Locate every blood parasite and identify its species.
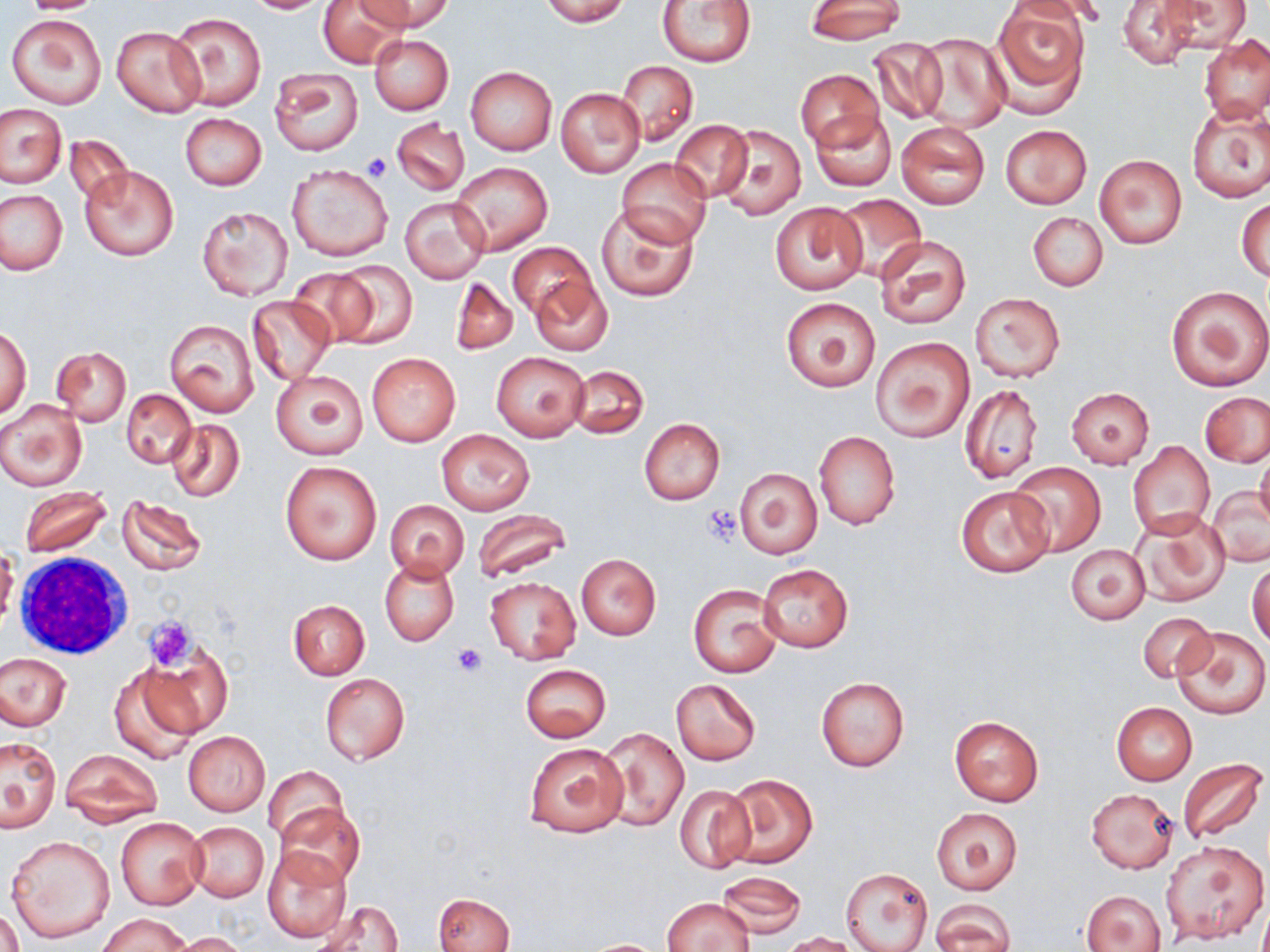

No blood parasites observed.

Approximate bounding boxes as [x1, y1, x2, y2] in pixels. Uninfected red blood cell locations: [18, 0, 105, 13], [242, 0, 334, 14], [363, 0, 452, 34], [538, 0, 629, 26], [806, 0, 905, 44], [992, 0, 1091, 107], [1004, 0, 1111, 27], [1117, 0, 1204, 70], [1160, 0, 1250, 53], [318, 1, 404, 68], [656, 1, 758, 68], [169, 12, 268, 111], [6, 13, 107, 108], [112, 26, 206, 117], [1200, 33, 1270, 123], [369, 34, 452, 116], [917, 34, 1008, 132], [868, 36, 949, 125], [617, 60, 697, 145], [466, 66, 556, 155], [270, 68, 364, 156], [796, 70, 883, 149], [557, 88, 645, 177], [1187, 103, 1270, 202], [1, 105, 65, 188], [811, 110, 897, 193], [180, 113, 266, 190], [392, 118, 471, 196], [669, 119, 754, 204], [895, 121, 989, 209], [713, 124, 807, 220], [999, 124, 1092, 210], [65, 134, 134, 209], [1093, 153, 1187, 248], [616, 157, 713, 249], [451, 162, 553, 255], [286, 163, 395, 262], [79, 164, 179, 261], [0, 189, 67, 275], [834, 195, 925, 278], [400, 196, 491, 283], [1237, 198, 1269, 281], [769, 202, 867, 294], [597, 205, 697, 300], [198, 206, 294, 301], [1028, 212, 1108, 292], [876, 235, 971, 329], [507, 242, 597, 325], [330, 262, 417, 348], [287, 268, 383, 348], [529, 275, 612, 358], [450, 277, 517, 355], [1166, 285, 1270, 391], [971, 293, 1064, 382], [248, 295, 335, 384], [780, 297, 880, 391], [164, 318, 260, 417], [1, 324, 31, 419], [870, 336, 975, 441], [52, 346, 132, 426], [491, 352, 589, 441], [367, 353, 459, 446], [568, 365, 648, 438], [271, 370, 369, 460], [960, 383, 1042, 483], [1067, 388, 1154, 468], [122, 390, 196, 468], [1201, 392, 1270, 467], [0, 399, 87, 491], [639, 418, 724, 505], [167, 419, 245, 503], [436, 429, 534, 515], [813, 432, 900, 529], [1128, 441, 1215, 537], [1255, 449, 1270, 532], [279, 460, 381, 565], [1007, 462, 1106, 557], [734, 468, 822, 560], [954, 485, 1055, 578], [18, 486, 112, 558], [1207, 487, 1270, 567], [116, 497, 206, 576], [384, 500, 468, 580], [472, 509, 573, 582], [1133, 513, 1230, 608], [1066, 544, 1150, 625], [0, 549, 18, 630], [575, 554, 661, 640], [381, 559, 458, 645], [1248, 560, 1270, 649], [758, 563, 854, 652], [484, 577, 580, 663], [688, 584, 783, 678], [288, 599, 370, 679], [1136, 612, 1216, 683], [1169, 624, 1270, 720], [139, 648, 230, 740], [1, 652, 72, 730], [520, 664, 612, 742], [108, 666, 202, 765], [320, 673, 409, 765], [816, 677, 908, 772], [670, 678, 761, 765], [1111, 702, 1197, 785], [950, 716, 1044, 806], [600, 728, 688, 831], [183, 731, 270, 816], [0, 737, 61, 830], [524, 743, 628, 839], [61, 749, 164, 827], [1176, 758, 1268, 845], [262, 766, 348, 846], [722, 774, 817, 868], [673, 784, 755, 873], [1085, 788, 1179, 873], [275, 801, 364, 887], [931, 808, 1022, 894], [117, 817, 206, 909], [186, 821, 270, 901], [5, 835, 114, 944], [1161, 839, 1268, 945], [262, 846, 351, 943], [840, 866, 933, 952], [717, 871, 805, 938], [1082, 889, 1167, 952], [433, 893, 514, 952], [662, 898, 754, 951], [930, 900, 1015, 952], [315, 901, 403, 952], [0, 909, 24, 952], [97, 913, 191, 952], [172, 932, 253, 952], [779, 932, 862, 952], [580, 939, 671, 951]. Platelet locations: [362, 153, 393, 181], [701, 506, 742, 547], [143, 617, 196, 671], [453, 644, 488, 676]. White blood cell locations: [13, 555, 132, 660]. Slide-level diagnosis: negative for blood parasites. May-Grünwald-Giemsa-stained preparation. Image is 1270×952 pixels. One field of a larger specimen. Captured at 1000x magnification. Thin blood film. Light microscopy.